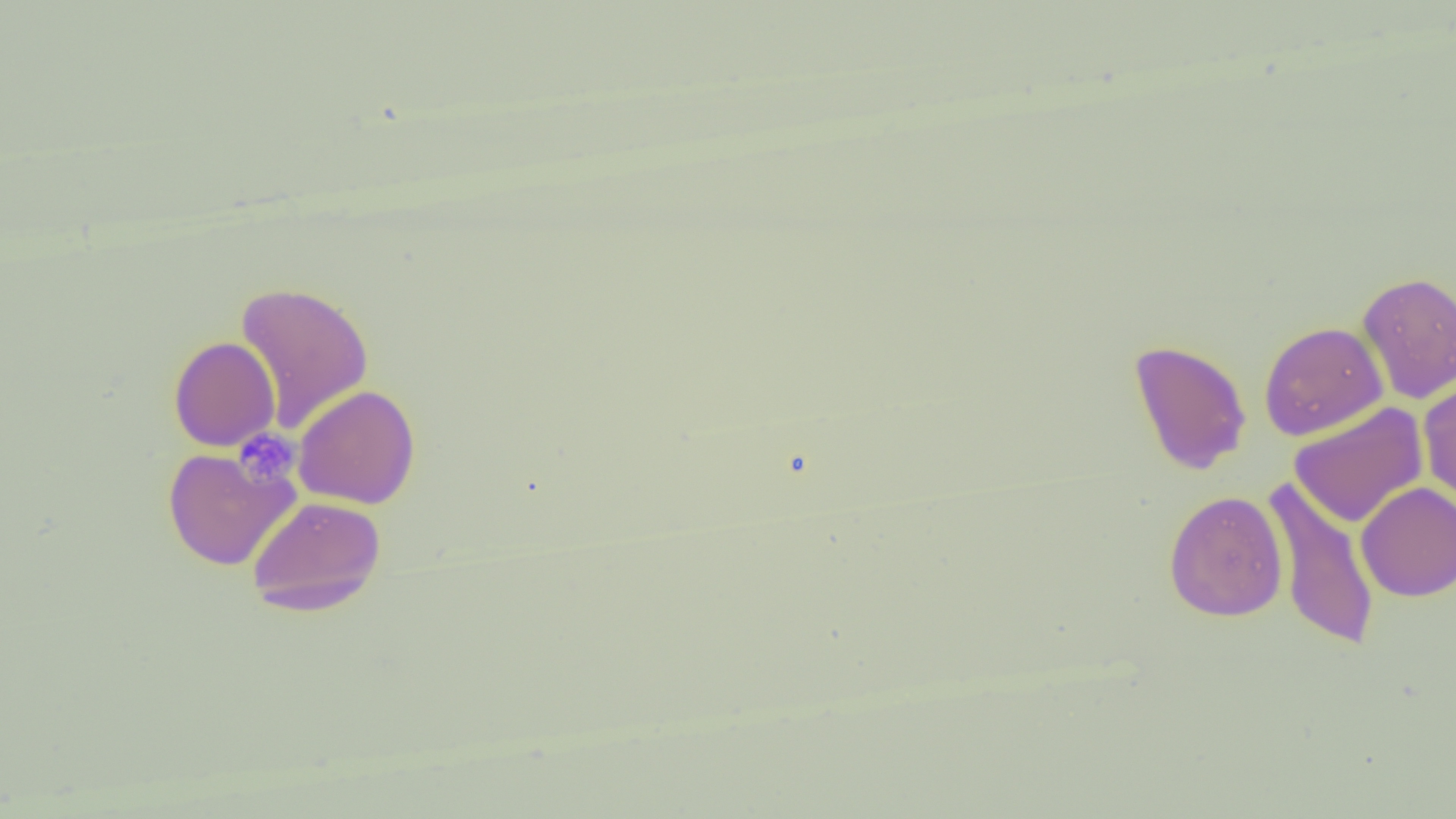
slide-level diagnosis = negative for blood parasites
image size = 1456×819 pixels
uninfected red blood cell locations = approximate bounding boxes as (x1,y1)-(x2,y2) corner pairs in pixels: (1356,271)-(1456,403), (235,281)-(374,433), (1259,321)-(1388,441), (168,336)-(280,452), (1128,339)-(1252,476), (1418,376)-(1456,508), (293,384)-(421,509), (1289,402)-(1428,528), (161,447)-(299,571), (1263,476)-(1381,652), (1355,481)-(1456,601), (1164,490)-(1288,622), (247,496)-(386,616)
field of view = one of a larger specimen
platelet locations = approximate bounding boxes as (x1,y1)-(x2,y2) corner pairs in pixels: (235,430)-(299,487)
preparation = thin blood film
modality = optical microscopy
magnification = 1000x